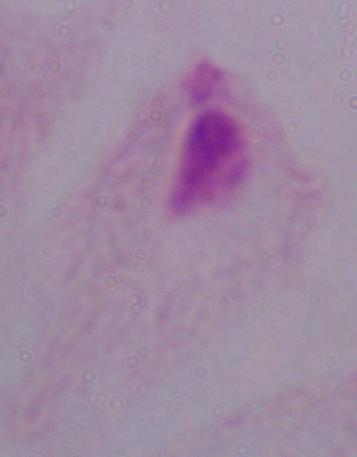
Summary:
  - Modality: micrograph
  - Identification: trichomonad
  - Magnification: 1000x